Locate and identify every blood parasite.
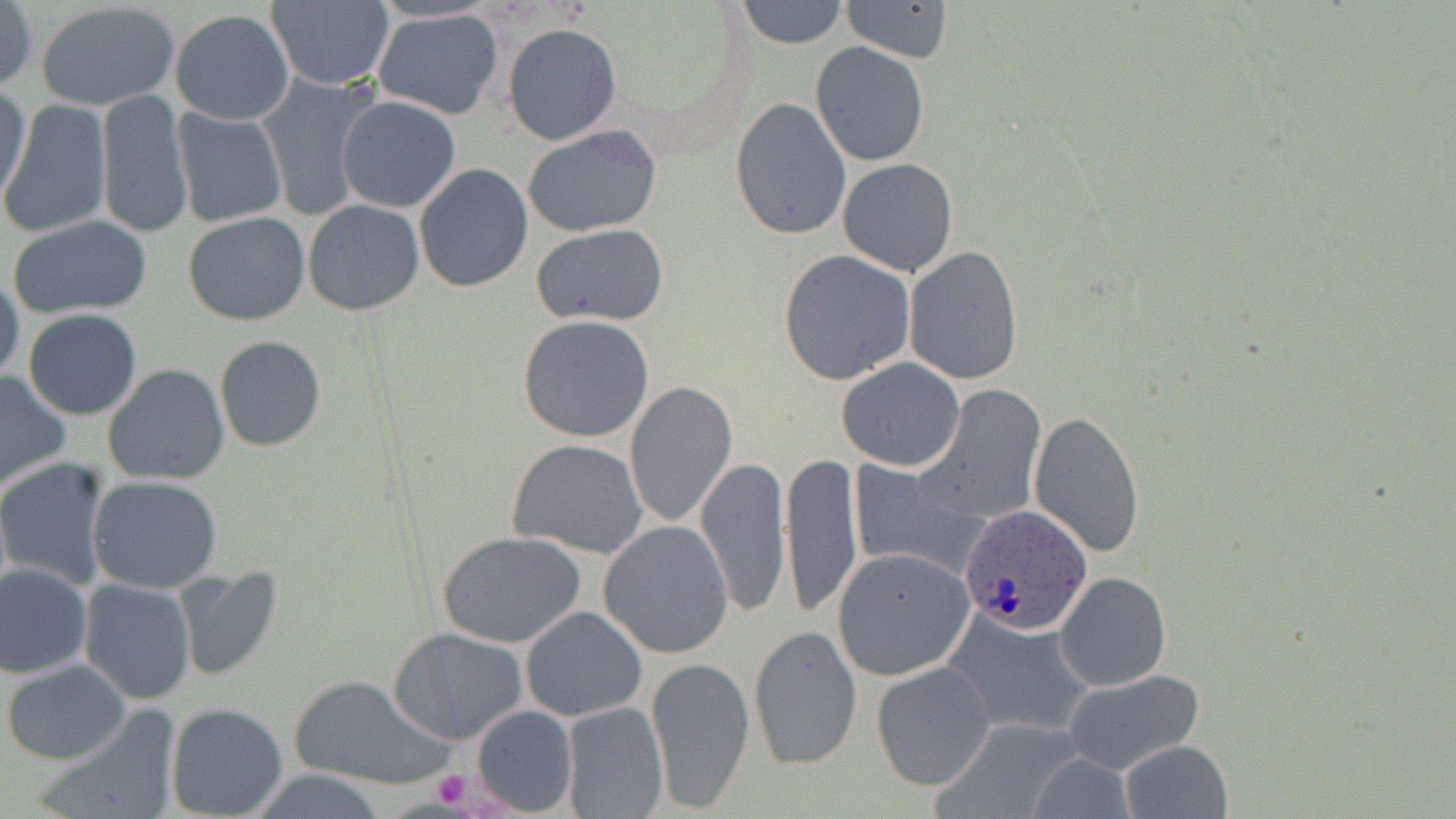

Approximate bounding boxes as (x1,y1)-(x2,y2) corner pairs in pixels.
Plasmodium ovale-infected red blood cells: (959,501)-(1091,633).
No Plasmodium falciparum, Plasmodium malariae, Plasmodium vivax, Babesia divergens, or Trypanosoma brucei observed.

Uninfected red blood cell locations: (0,0)-(38,93), (736,0)-(850,49), (36,1)-(181,110), (265,1)-(395,90), (842,1)-(952,62), (372,8)-(504,121), (169,9)-(294,125), (504,24)-(621,144), (809,42)-(930,167), (257,73)-(384,224), (0,81)-(32,209), (95,88)-(194,239), (335,96)-(461,213), (729,99)-(853,239), (1,102)-(111,238), (171,107)-(286,228), (522,125)-(663,238), (838,158)-(958,278), (413,163)-(534,292), (302,201)-(424,316), (183,213)-(311,326), (7,215)-(154,319), (534,225)-(668,327), (903,246)-(1023,385), (778,250)-(916,384), (0,270)-(24,386), (22,309)-(143,420), (517,315)-(657,442), (214,335)-(327,453), (836,358)-(965,471), (103,363)-(231,486), (0,369)-(73,491), (624,381)-(738,528), (917,384)-(1046,526), (1029,410)-(1145,558), (508,438)-(647,559), (781,453)-(862,617), (695,455)-(792,617), (0,458)-(115,592), (848,461)-(988,581), (88,475)-(222,591), (599,520)-(734,658), (437,531)-(586,648), (832,548)-(974,681), (0,562)-(93,678), (173,566)-(283,681), (0,568)-(182,689), (1056,571)-(1171,690), (78,580)-(196,703), (519,606)-(647,721), (944,607)-(1093,739), (749,624)-(861,771), (389,628)-(528,745), (647,654)-(754,812), (2,659)-(130,765), (872,661)-(994,789), (1063,669)-(1204,774), (292,673)-(451,790), (560,701)-(669,818), (166,702)-(289,818), (470,705)-(577,815), (35,706)-(179,819), (1117,739)-(1234,819), (247,770)-(386,819). Platelet locations: (430,769)-(471,811). Slide-level diagnosis: Plasmodium ovale. Thin blood smear. Light microscopy. Single field of view. May-Grünwald-Giemsa-stained preparation. Image is 1456×819 pixels. 1000x magnification.